Report the malaria status of this cell.
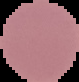

Uninfected.

image size = 79×82 pixels
image type = cell region segmented out of the field of view; surrounding area masked to black
preparation = thin blood film